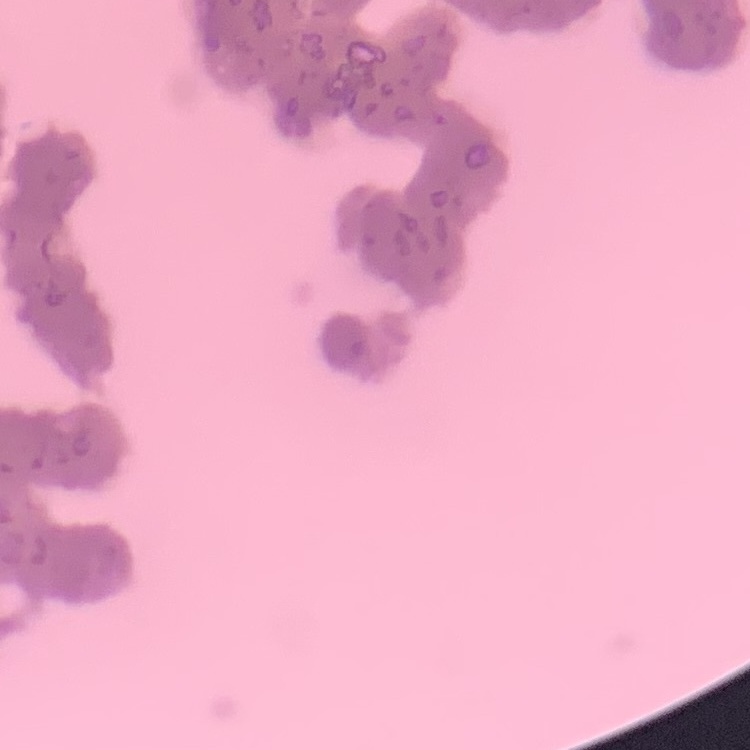 The erythrocytes show rouleaux formation. Thin peripheral smear. Square crop of a larger photomicrograph. Stained with either Field's or Giemsa.